Classify this cell by malaria status.
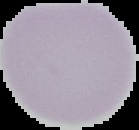
Uninfected.

From a thin blood smear. Image is 139×130 pixels. Cell region segmented out of the field of view; the surrounding area is masked to black.